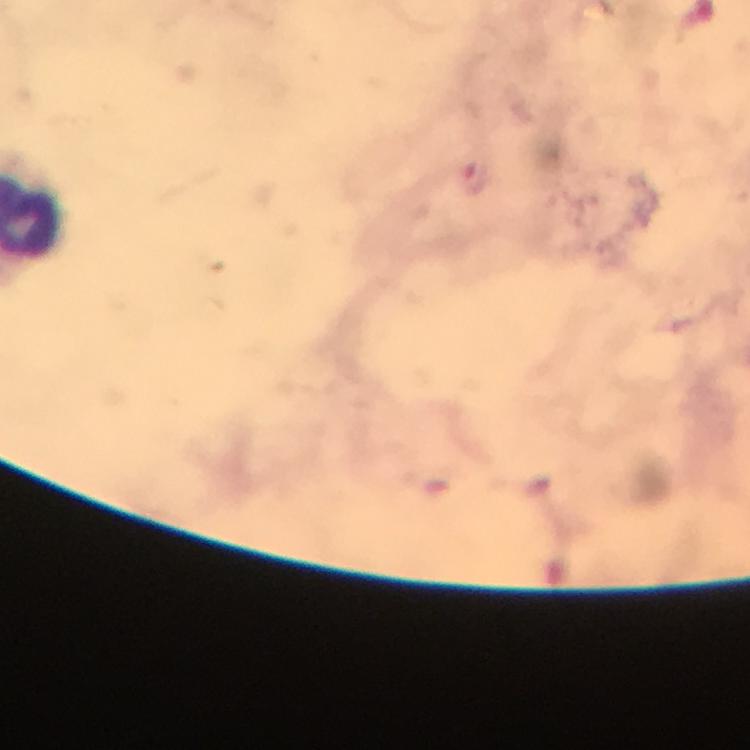
Approximate centers as {x, y} in pixels.
Summary:
  - Plasmodium parasite locations: {477, 178}
  - Image size: 750×750 pixels
  - Immersion oil: applied
  - Capture: smartphone mounted on the microscope
  - Magnification: 100x
  - Context: from a diagnostic examination for malaria
  - Stain: Giemsa
  - Preparation: thick blood film
  - Cropped from: a single field of view